Report the malaria status of this cell.
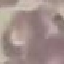

Uninfected.

stain = Giemsa
preparation = thin blood film
image type = cell patch, automatically extracted from a larger field of view and resized to 64 × 64 pixels
capture = smartphone through the microscope eyepiece